Locate and identify every blood parasite.
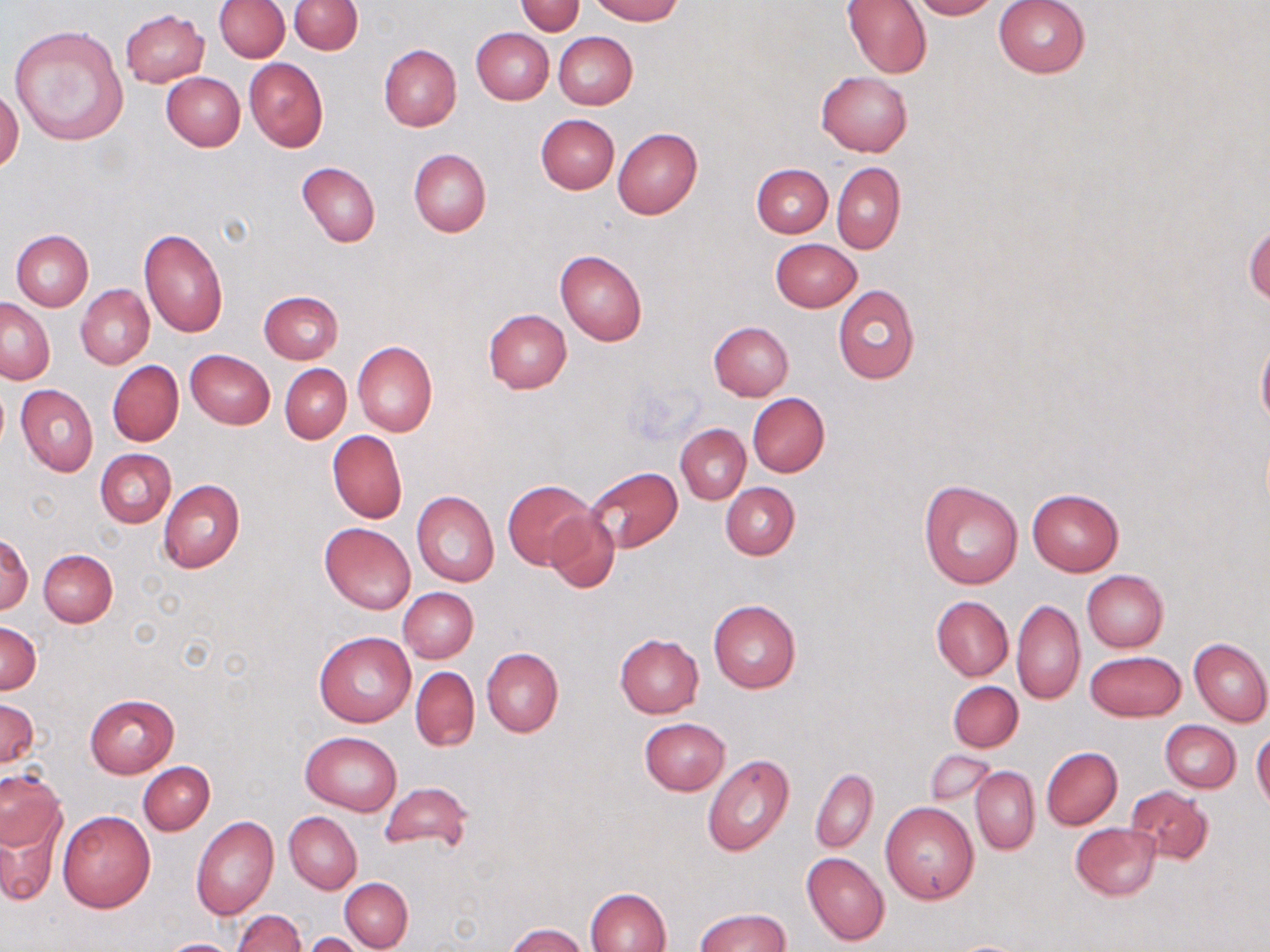

No blood parasites observed.

Approximate bounding boxes as (x1, y1, x2, y2) in pixels. Uninfected red blood cell locations: (290, 0, 361, 55), (591, 0, 682, 24), (842, 0, 931, 79), (910, 0, 1001, 20), (993, 0, 1090, 78), (215, 1, 288, 61), (517, 2, 584, 35), (120, 8, 209, 87), (9, 24, 130, 147), (471, 28, 553, 105), (553, 31, 638, 109), (379, 44, 461, 131), (244, 58, 328, 152), (161, 72, 245, 151), (816, 72, 913, 157), (0, 88, 23, 174), (535, 114, 619, 193), (612, 128, 702, 220), (409, 149, 491, 237), (297, 162, 380, 248), (832, 162, 906, 254), (751, 163, 832, 238), (1246, 218, 1269, 310), (138, 229, 227, 337), (11, 230, 92, 311), (769, 238, 861, 312), (555, 249, 647, 346), (75, 285, 154, 369), (833, 285, 920, 385), (259, 291, 344, 365), (1, 298, 53, 385), (483, 309, 572, 393), (708, 321, 793, 400), (1256, 334, 1270, 432), (352, 341, 437, 437), (185, 349, 274, 428), (107, 360, 184, 447), (281, 364, 352, 443), (16, 385, 99, 477), (747, 392, 829, 477), (676, 425, 750, 504), (327, 429, 407, 523), (95, 449, 176, 528), (584, 467, 682, 552), (159, 480, 245, 573), (503, 480, 594, 570), (919, 480, 1026, 589), (721, 481, 799, 559), (1026, 489, 1124, 576), (411, 491, 499, 588), (543, 508, 620, 593), (320, 522, 415, 614), (0, 533, 31, 615), (39, 548, 117, 627), (1082, 570, 1168, 652), (398, 587, 478, 663), (931, 595, 1012, 682), (708, 598, 802, 693), (1012, 600, 1084, 705), (1, 623, 41, 694), (313, 630, 416, 727), (615, 633, 705, 718), (1189, 638, 1270, 727), (481, 649, 562, 737), (1085, 649, 1186, 722), (411, 666, 479, 751), (948, 681, 1023, 752), (85, 694, 177, 778), (0, 700, 39, 769), (640, 718, 730, 795), (1160, 720, 1241, 793), (301, 731, 401, 815), (1252, 731, 1270, 811), (1042, 747, 1123, 830), (924, 750, 994, 805), (702, 753, 795, 858), (138, 761, 215, 835), (971, 767, 1039, 855), (811, 769, 878, 854), (0, 770, 65, 855), (380, 782, 472, 853), (1125, 786, 1214, 866), (880, 802, 980, 904), (56, 809, 156, 912), (285, 812, 361, 893), (191, 815, 279, 920), (1, 817, 58, 905), (1071, 822, 1161, 900), (802, 852, 890, 946), (339, 878, 413, 951), (585, 887, 671, 952), (695, 907, 790, 952), (232, 910, 306, 952), (504, 923, 587, 952), (302, 932, 367, 952), (157, 938, 241, 952). Slide-level diagnosis: no evidence of blood parasites. 1000x magnification. Light microscopy. Thin blood smear. May-Grünwald-Giemsa-stained preparation. One field of a larger specimen. Image is 1270×952 pixels.